Name the parasite shown.
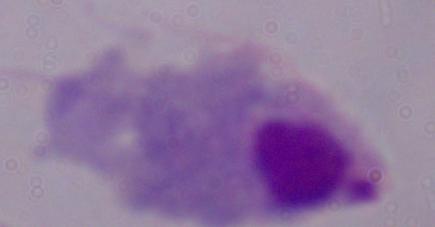

A trichomonad.

magnification = 1000x
modality = micrograph